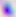
modality: photomicrograph
magnification: 400x
identification: Toxoplasma gondii